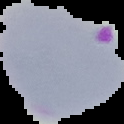
Summary:
  - Image type: segmented cell region with the area outside set to black
  - Preparation: thin blood smear
  - Image size: 124×124 pixels
  - Result: Plasmodium parasites identified